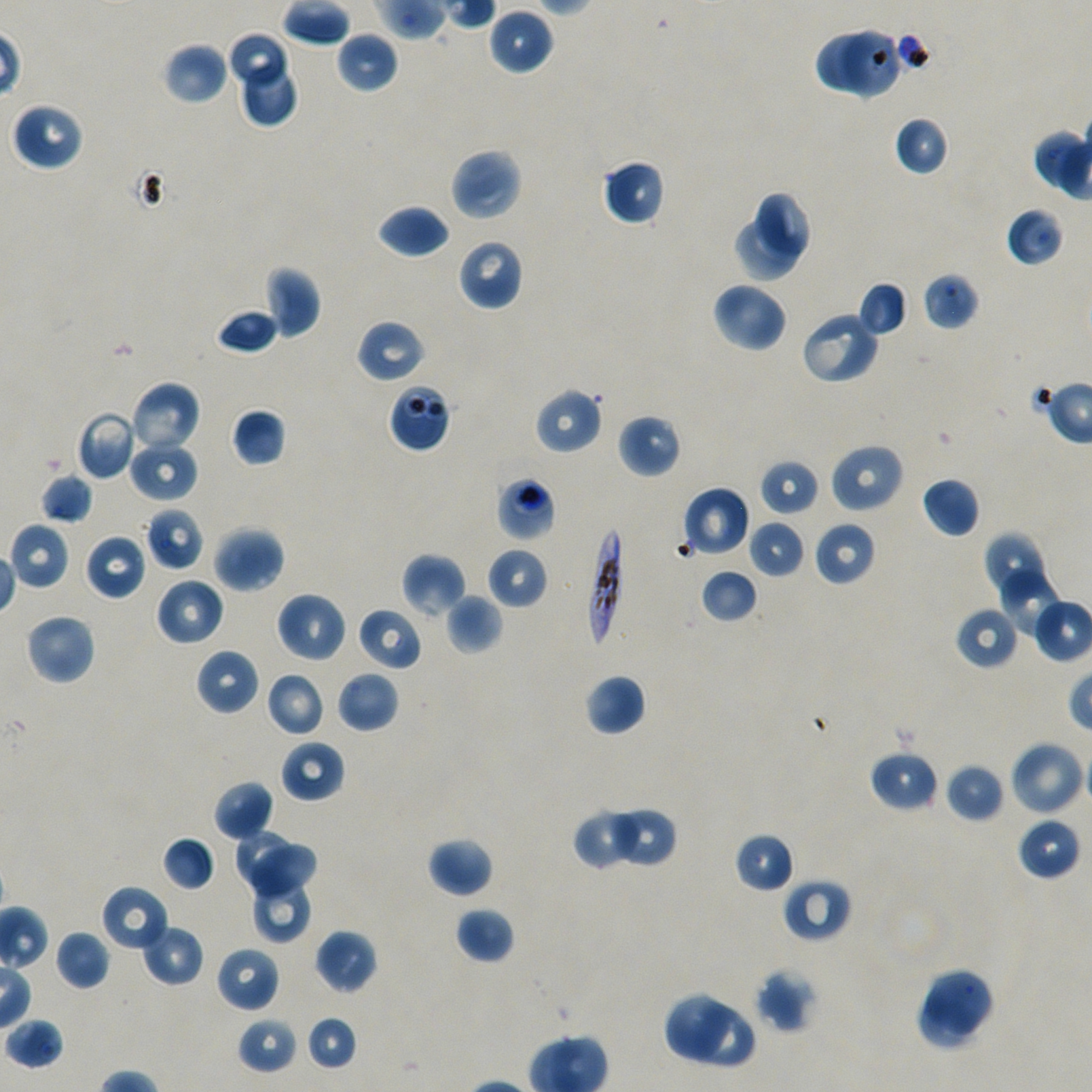
Approximate bounding boxes as (x1, y1, x2, y2) in pixels. Not every red blood cell is marked.
Summary:
  - Locations of uninfected red blood cells: (489, 8, 553, 75), (226, 31, 287, 84), (335, 31, 398, 94), (162, 42, 229, 105), (239, 60, 300, 128), (11, 101, 84, 170), (893, 115, 950, 176), (450, 147, 523, 221), (601, 158, 666, 226), (755, 192, 813, 255), (377, 204, 450, 259), (1006, 207, 1065, 268), (733, 216, 802, 283), (456, 238, 525, 312), (265, 265, 321, 338), (922, 272, 979, 331), (710, 281, 788, 352), (858, 281, 908, 337), (217, 308, 279, 355), (801, 310, 880, 385), (357, 319, 426, 384), (129, 380, 202, 455), (534, 388, 602, 455), (230, 408, 286, 467), (75, 410, 139, 480), (617, 413, 682, 478), (128, 439, 199, 503), (829, 442, 905, 513), (760, 459, 819, 517), (39, 473, 94, 524), (922, 476, 981, 539), (681, 486, 751, 558), (145, 507, 204, 571), (747, 520, 807, 579), (813, 520, 877, 586), (8, 522, 71, 590), (213, 525, 285, 593), (982, 530, 1044, 596), (85, 533, 147, 601), (486, 547, 548, 608), (401, 553, 466, 619), (700, 568, 759, 624), (1001, 570, 1063, 639), (155, 577, 224, 647), (274, 591, 347, 664), (445, 594, 502, 654), (1032, 594, 1092, 662), (357, 606, 422, 672), (954, 606, 1019, 670), (24, 613, 96, 686), (195, 648, 260, 716), (335, 670, 399, 733), (266, 671, 326, 737), (585, 674, 647, 737), (280, 740, 346, 803), (1008, 740, 1085, 817), (869, 748, 939, 813), (945, 762, 1006, 824), (212, 780, 274, 841), (613, 806, 677, 865), (574, 812, 638, 868), (1016, 816, 1081, 881), (232, 829, 294, 888), (734, 832, 794, 892), (161, 835, 216, 892), (427, 836, 493, 897), (244, 844, 318, 896), (782, 877, 852, 943), (252, 880, 313, 944), (101, 885, 169, 953), (454, 906, 515, 965), (141, 924, 204, 986), (314, 928, 378, 995), (54, 929, 111, 990), (216, 945, 280, 1013), (926, 966, 996, 1038), (754, 968, 816, 1034), (917, 991, 975, 1051), (666, 994, 733, 1059), (689, 1006, 754, 1068), (305, 1015, 358, 1072), (236, 1016, 299, 1075), (4, 1017, 65, 1070)
  - Locations of red blood cells of indeterminate infection status: (840, 24, 898, 103), (816, 26, 880, 91), (386, 382, 452, 453), (495, 475, 556, 541)
  - Locations of infected red blood cells: (587, 526, 626, 648)
  - Preparation: thin blood film
  - Donor blood group: A+/O+
  - Culture: static in-vitro Plasmodium falciparum strain NF54
  - Stain: Giemsa
  - Image size: 1092×1092 pixels
  - Objective: 100x, oil immersion, numerical aperture 1.45
  - Field of view: single